Assess this cell for malaria.
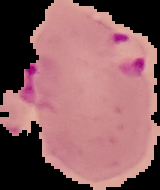

It is parasitized.

Summary:
  - Image type: segmented cell region with the area outside set to black
  - Image size: 160×190 pixels
  - Preparation: thin blood smear